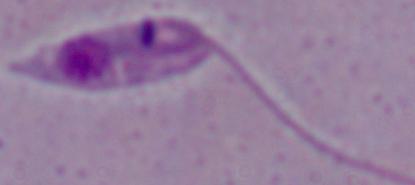

Summary:
  - Identification: Leishmania
  - Magnification: 1000x
  - Modality: photomicrograph